Name the cell type shown.
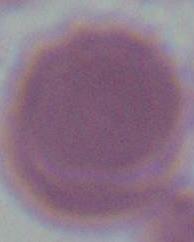

This is an erythrocyte.

Summary:
  - Modality: micrograph
  - Magnification: 1000x